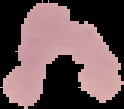

Result: Plasmodium parasites identified. Cell region segmented out of the field of view; the surrounding area is masked to black. Image is 124×109 pixels. From a thin blood smear.